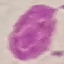 Result: no malaria parasites detected. Giemsa-stained preparation. Thin blood film. Acquired by smartphone through the microscope eyepiece. Cell patch, automatically extracted from a larger field of view and resized to 64 × 64 pixels.